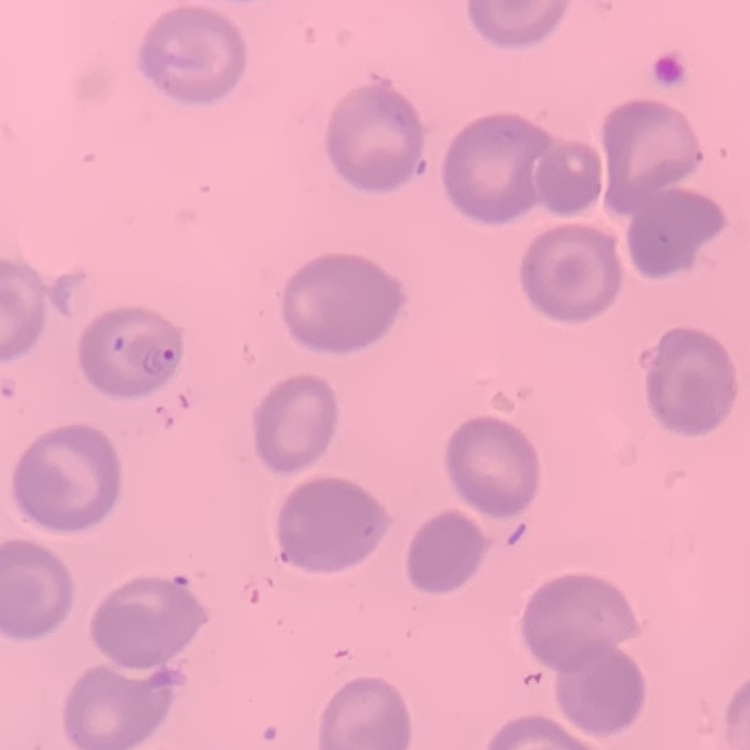

The red blood cells show no rouleaux formation. One tile cut from a larger photomicrograph. Thin blood smear. Field's or Giemsa stain.